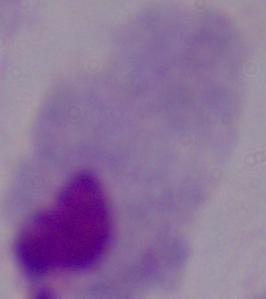

{
  "modality": "photomicrograph",
  "identification": "trichomonad",
  "magnification": "1000x"
}